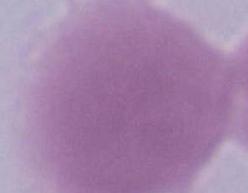

modality = photomicrograph
identification = red blood cell
magnification = 1000x